State which parasite is depicted.
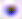

Toxoplasma gondii.

Photomicrograph. Captured at 400x magnification.